Classify this cell by malaria status.
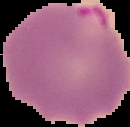
It is parasitized.

Summary:
  - Preparation: thin blood smear
  - Image size: 130×127 pixels
  - Image type: segmented cell region on a black background